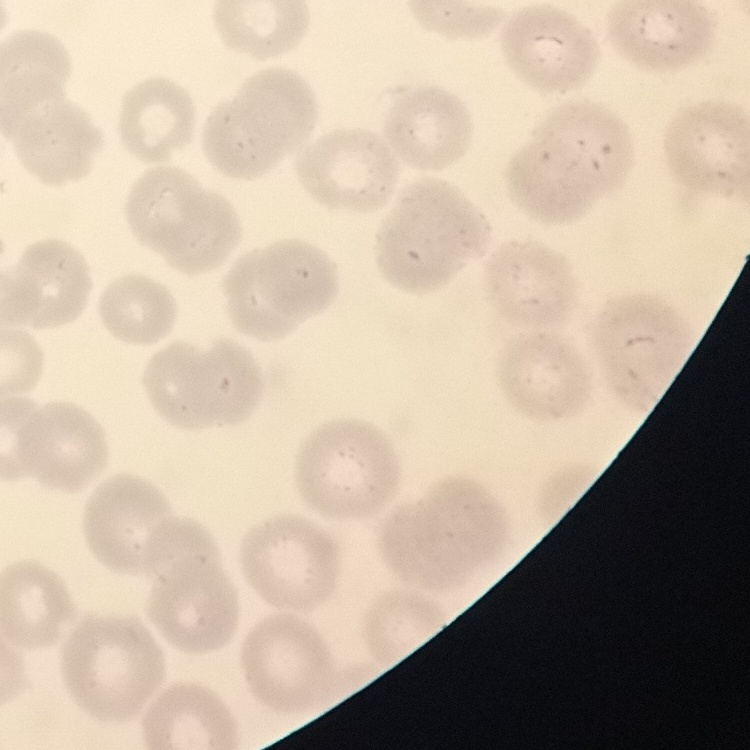 The erythrocytes show no rouleaux formation. Square crop of a larger photomicrograph. Thin blood smear. Stained with either Field's or Giemsa.